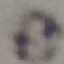
Summary:
  - Result: no malaria parasites seen
  - Image type: automatically extracted cell patch, resized to 64 × 64 pixels
  - Stain: Giemsa
  - Preparation: thin blood film
  - Capture: smartphone through the microscope eyepiece